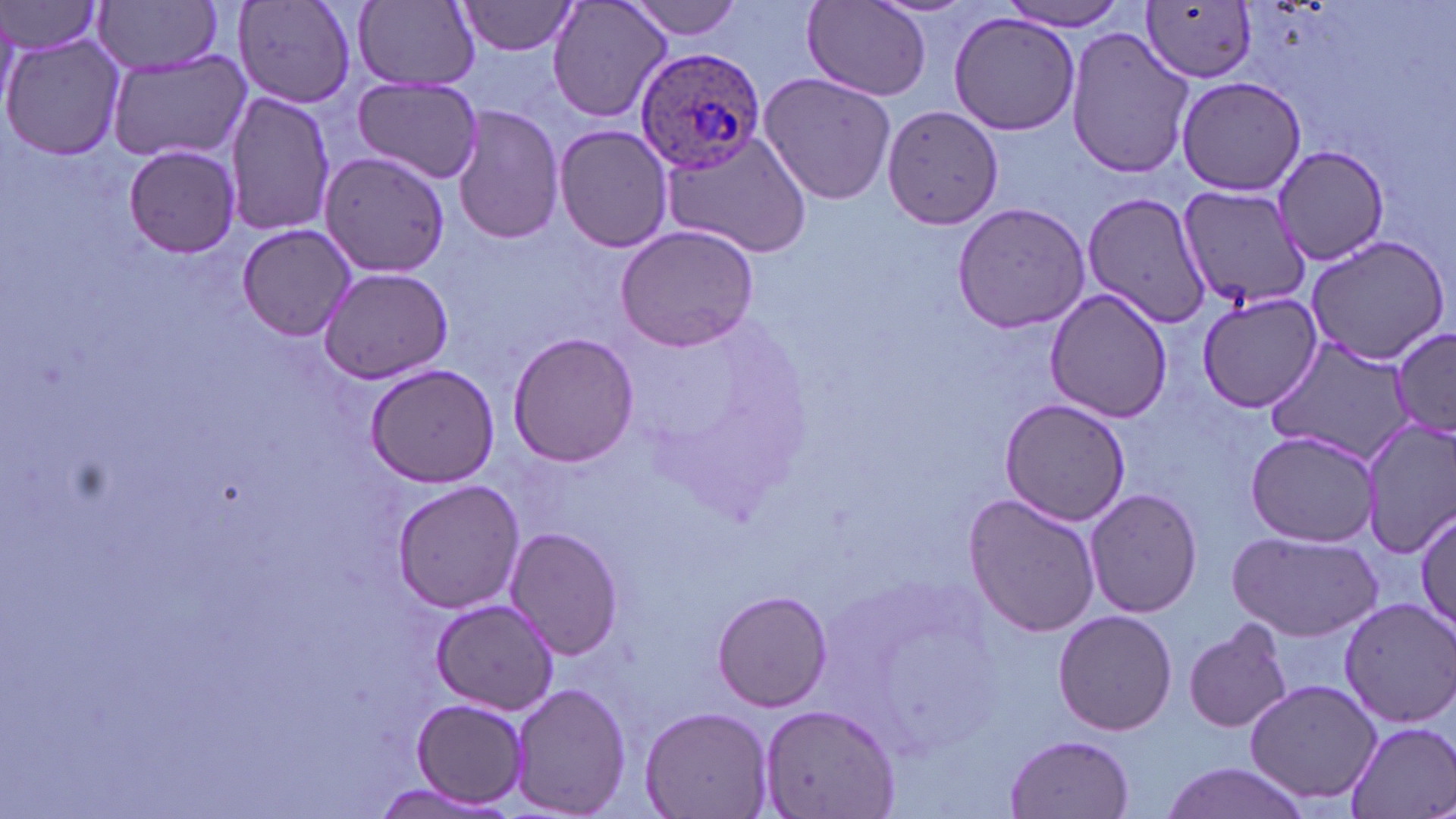 Approximate bounding boxes as (x1, y1, x2, y2) in pixels. Uninfected red blood cell locations: (95, 0, 225, 75), (233, 0, 358, 111), (356, 0, 480, 90), (547, 0, 672, 125), (621, 0, 747, 40), (455, 1, 581, 56), (1138, 1, 1255, 84), (0, 2, 106, 59), (803, 2, 931, 103), (995, 2, 1133, 32), (947, 12, 1080, 135), (1064, 26, 1194, 180), (3, 31, 125, 162), (106, 53, 252, 163), (757, 70, 896, 207), (352, 75, 484, 184), (223, 90, 335, 238), (452, 103, 566, 246), (883, 104, 1004, 229), (552, 125, 673, 255), (657, 131, 812, 260), (122, 144, 243, 259), (1259, 149, 1389, 273), (318, 150, 451, 278), (1176, 186, 1312, 311), (1083, 190, 1212, 328), (952, 201, 1092, 335), (235, 224, 358, 342), (614, 224, 761, 353), (1302, 234, 1450, 366), (318, 266, 456, 385), (1045, 287, 1174, 423), (1193, 288, 1326, 412), (1393, 325, 1456, 438), (506, 331, 639, 468), (1266, 334, 1415, 463), (364, 362, 500, 488), (999, 397, 1133, 525), (1361, 417, 1456, 559), (1244, 429, 1383, 546), (392, 479, 526, 614), (1084, 489, 1203, 618), (961, 494, 1100, 637), (1415, 508, 1455, 633), (506, 527, 624, 659), (1226, 528, 1384, 642), (712, 590, 833, 711), (1339, 597, 1456, 727), (431, 599, 560, 715), (1053, 609, 1177, 736), (1184, 618, 1296, 734), (1245, 678, 1384, 808), (510, 681, 629, 816), (411, 698, 529, 808), (759, 701, 900, 818), (642, 704, 773, 817), (1344, 719, 1453, 819), (1006, 733, 1135, 817), (1153, 760, 1318, 819), (369, 780, 508, 816). Plasmodium ovale-infected red blood cell locations: (634, 45, 768, 170). Slide-level diagnosis: Plasmodium ovale. Captured at 1000x magnification. Light microscopy. Thin blood smear. May-Grünwald-Giemsa stain. Single field of view. Image is 1456×819 pixels.